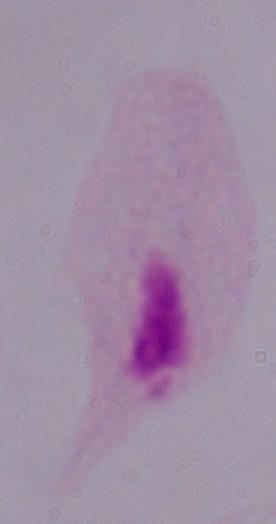
identification = trichomonad
modality = photomicrograph
magnification = 1000x